Evaluate for parasitized red blood cells.
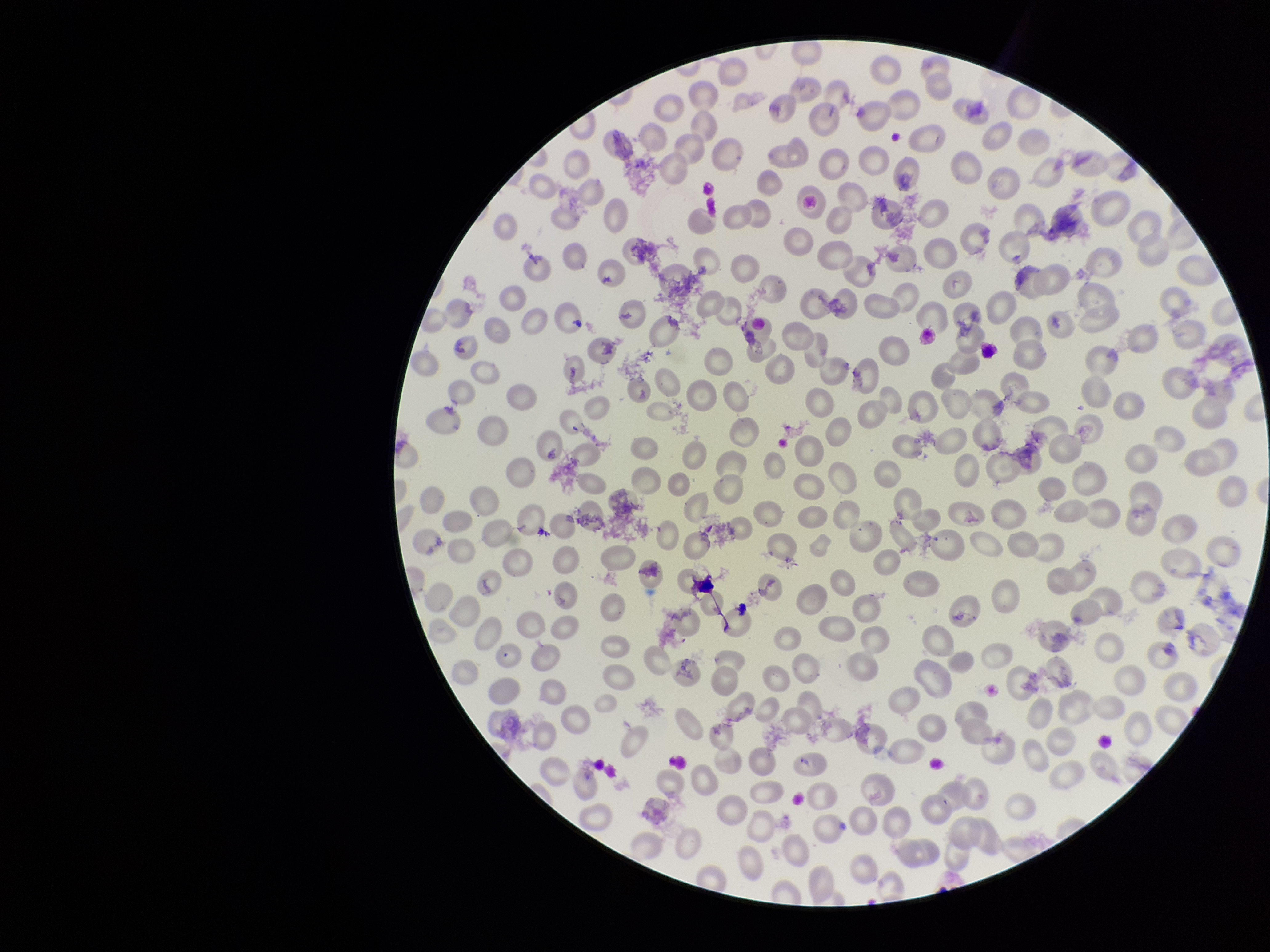
None identified.

capture = smartphone photograph through the microscope eyepiece
preparation = thin blood smear
parasitized red blood cell count = 0
patient malaria status = positive
red blood cell count = 262
species reported for this patient = Plasmodium vivax
stain = Giemsa
image size = 1270×952 pixels
field of view = one from this slide